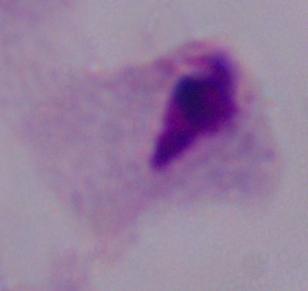
Summary:
  - Magnification: 1000x
  - Modality: micrograph
  - Identification: trichomonad